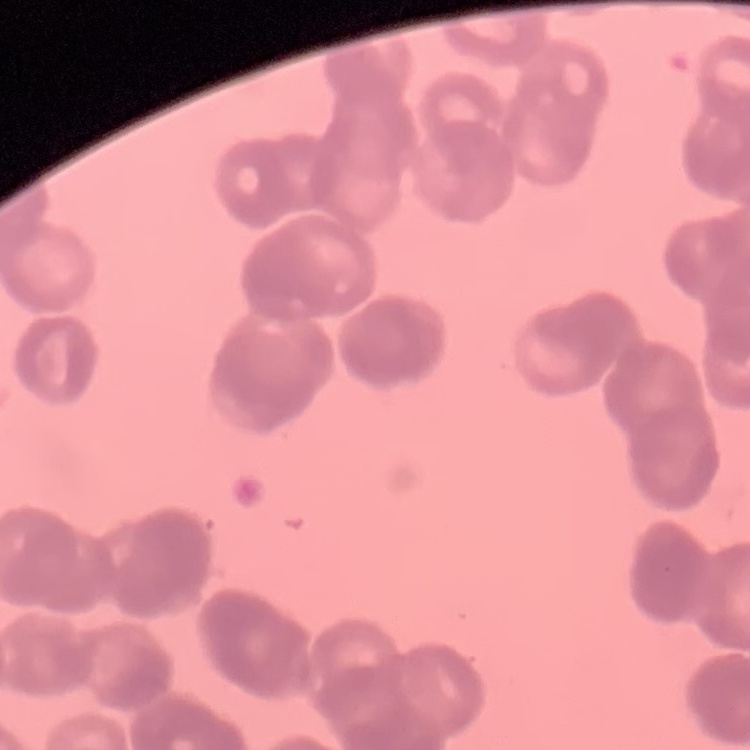

{
  "red_blood_cell_morphology": "rouleaux formation",
  "preparation": "thin blood smear",
  "stain": "Field's or Giemsa",
  "image_type": "square crop of a larger photomicrograph"
}